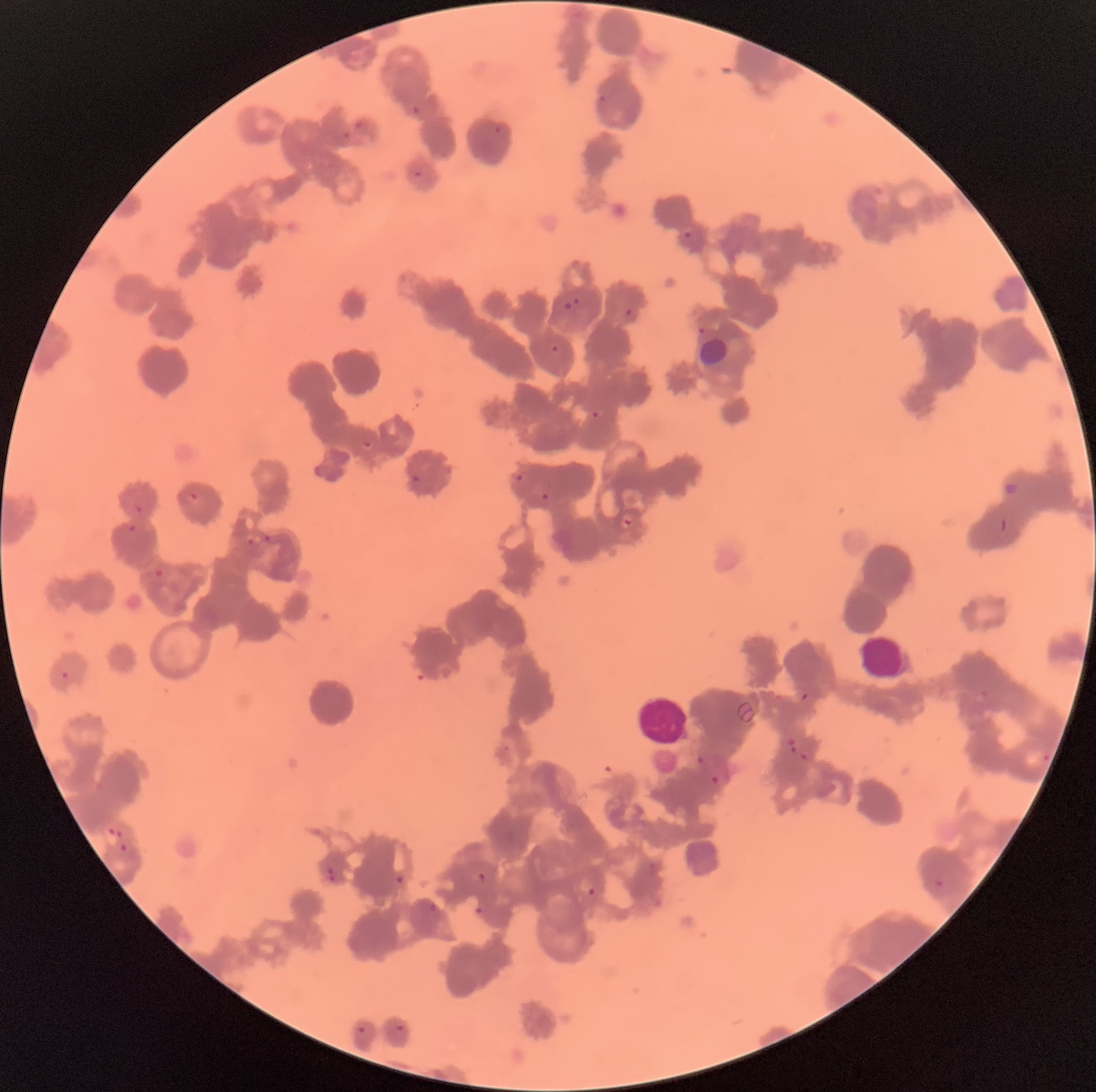
{
  "white_blood_cell_locations": "approximate bounding boxes as [x1, y1, x2, y2] in pixels: [635, 694, 689, 746]",
  "preparation": "thin blood smear",
  "plasmodium_parasite_locations": "approximate bounding boxes as [x1, y1, x2, y2] in pixels: [598, 94, 606, 103], [411, 105, 421, 116], [354, 121, 362, 129], [493, 126, 502, 135], [343, 131, 351, 140], [413, 170, 423, 178], [683, 231, 691, 239], [573, 297, 581, 305], [562, 302, 573, 312], [623, 308, 632, 316], [698, 327, 706, 336], [551, 345, 559, 353], [591, 411, 600, 419], [363, 441, 374, 450], [411, 474, 420, 483], [514, 474, 525, 482], [1004, 482, 1020, 497], [541, 492, 550, 500], [189, 493, 199, 503], [134, 506, 144, 514], [620, 514, 636, 528], [126, 524, 137, 532], [263, 534, 272, 543], [246, 537, 254, 546], [154, 568, 165, 579], [858, 635, 909, 683], [60, 671, 69, 680], [800, 691, 810, 701], [787, 739, 797, 754], [799, 753, 810, 761], [1044, 754, 1050, 763], [695, 755, 708, 765], [711, 774, 721, 785], [107, 827, 123, 839], [119, 843, 128, 853], [326, 867, 338, 883], [471, 872, 487, 883], [394, 875, 406, 885], [934, 879, 946, 889], [587, 885, 598, 897], [429, 902, 439, 912], [475, 905, 485, 917], [395, 1023, 405, 1033], [357, 1026, 366, 1034]",
  "image_size": "1096×1092 pixels",
  "modality": "light microscopy",
  "red_blood_cell_morphology": "rouleaux formation"
}